State which parasite is depicted.
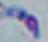

Toxoplasma gondii.

magnification = 1000x
modality = photomicrograph